Report the malaria status of this cell.
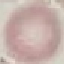
Uninfected.

Thin smear of blood. Acquired by smartphone through the microscope eyepiece. Automatically extracted cell patch, resized to 64 × 64 pixels. Giemsa-stained preparation.